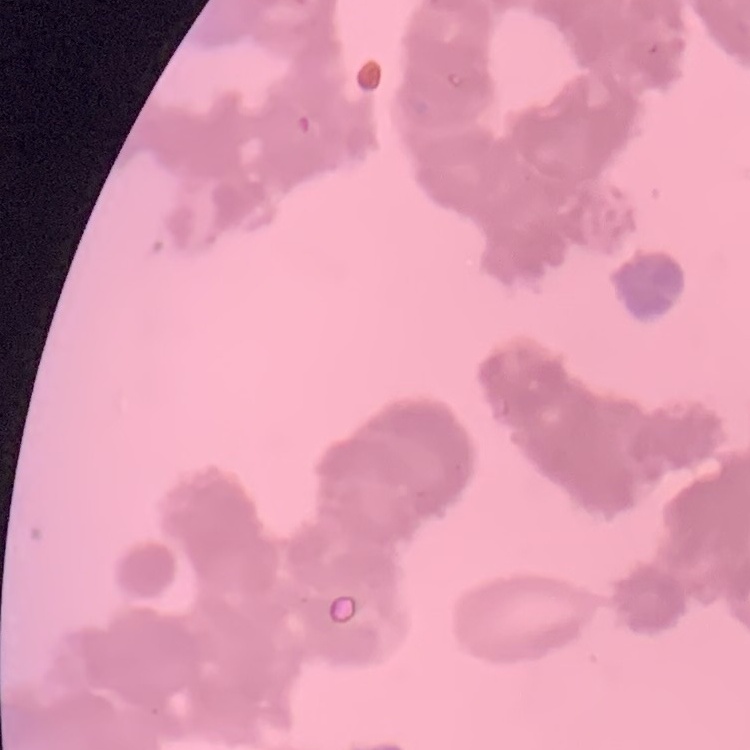
The erythrocytes show rouleaux formation. One tile cut from a larger photomicrograph. Stained with either Field's or Giemsa. Thin blood smear.